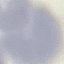

Summary:
  - Malaria status: uninfected
  - Capture: smartphone through the microscope eyepiece
  - Stain: Giemsa
  - Preparation: thin blood film
  - Image type: automatically extracted cell patch, resized to 64 × 64 pixels